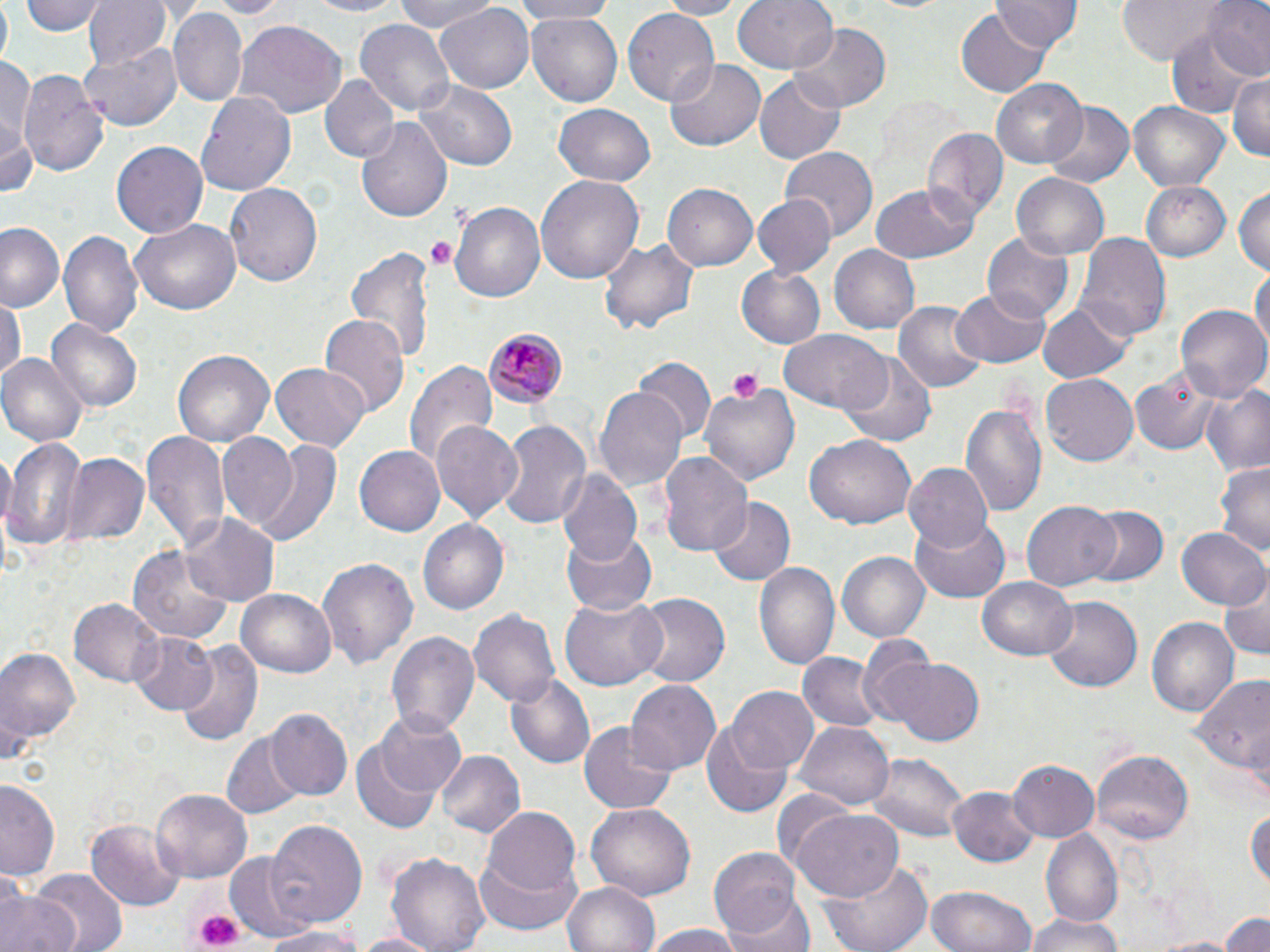
slide-level diagnosis = Plasmodium malariae
stain = May-Grünwald-Giemsa
field of view = one of a larger specimen
preparation = thin blood smear
magnification = 1000x
Plasmodium malariae-infected red blood cell locations = approximate bounding boxes as (x1,y1)-(x2,y2) corner pairs in pixels: (482,326)-(566,409)
modality = light microscopy
platelet locations = approximate bounding boxes as (x1,y1)-(x2,y2) corner pairs in pixels: (425,235)-(459,270), (726,368)-(762,402), (191,905)-(243,949)
image size = 1270×952 pixels
uninfected red blood cell locations = approximate bounding boxes as (x1,y1)-(x2,y2) corner pairs in pixels: (23,0)-(105,37), (83,0)-(169,71), (199,0)-(293,18), (296,0)-(411,17), (393,0)-(497,33), (508,0)-(625,22), (658,0)-(741,18), (733,0)-(838,75), (993,0)-(1081,54), (1115,0)-(1225,65), (1202,0)-(1270,80), (436,3)-(532,92), (171,7)-(248,107), (957,7)-(1052,95), (624,9)-(721,107), (527,12)-(623,109), (235,19)-(347,119), (355,19)-(454,114), (1166,22)-(1258,114), (791,25)-(891,111), (80,40)-(181,133), (0,57)-(33,146), (666,58)-(765,151), (19,68)-(108,177), (1225,72)-(1270,160), (756,73)-(846,165), (320,74)-(397,165), (991,77)-(1089,168), (414,78)-(516,171), (196,89)-(297,197), (1128,100)-(1230,191), (1041,103)-(1134,190), (551,104)-(657,188), (2,112)-(37,200), (357,117)-(452,225), (922,126)-(1006,225), (112,140)-(208,240), (780,146)-(879,239), (1012,172)-(1111,260), (536,173)-(642,284), (226,180)-(323,289), (1142,180)-(1229,261), (870,182)-(981,264), (664,185)-(757,271), (1233,185)-(1270,279), (753,196)-(834,276), (451,201)-(545,305), (130,220)-(242,315), (1,224)-(65,311), (58,228)-(143,339), (983,233)-(1076,319), (598,234)-(699,338), (1076,234)-(1169,345), (345,245)-(437,364), (829,246)-(920,334), (1253,265)-(1269,360), (736,266)-(826,349), (949,287)-(1049,369), (0,294)-(23,387), (1037,301)-(1133,384), (894,302)-(985,395), (1176,303)-(1269,400), (319,314)-(409,419), (48,320)-(144,413), (778,329)-(891,412), (174,347)-(274,447), (838,352)-(941,448), (0,354)-(87,449), (632,358)-(714,445), (404,361)-(495,470), (270,362)-(371,451), (1128,363)-(1230,456), (1040,374)-(1138,466), (700,380)-(800,488), (1201,383)-(1270,477), (595,387)-(689,493), (962,403)-(1046,513), (495,419)-(592,533), (431,420)-(525,519), (139,430)-(232,551), (215,431)-(300,523), (805,432)-(918,530), (229,434)-(342,548), (4,439)-(85,551), (355,448)-(445,535), (659,451)-(753,561), (62,454)-(148,548), (903,462)-(992,553), (1216,463)-(1269,559), (556,470)-(642,566), (710,497)-(794,587), (1023,500)-(1121,589), (1080,504)-(1168,588), (185,515)-(278,604), (910,515)-(1011,601), (419,519)-(508,614), (1176,526)-(1267,612), (560,527)-(660,616), (130,543)-(234,642), (835,550)-(928,643), (317,556)-(416,674), (755,559)-(841,673), (1220,572)-(1270,661), (978,575)-(1076,660), (236,588)-(337,678), (635,592)-(730,687), (1043,594)-(1142,694), (560,597)-(666,690), (71,598)-(163,689), (469,607)-(560,707), (1147,616)-(1238,714), (387,627)-(479,737), (129,630)-(220,716), (857,636)-(940,726), (173,639)-(264,751), (0,643)-(82,753), (799,650)-(884,732), (884,658)-(983,744), (1184,669)-(1268,789), (504,673)-(595,769), (626,679)-(720,776), (729,685)-(815,769), (265,710)-(352,802), (373,710)-(468,797), (701,720)-(794,818), (580,721)-(677,814), (796,721)-(894,809), (221,730)-(306,819), (352,739)-(446,836), (436,749)-(526,838), (1091,750)-(1193,843), (866,751)-(973,842), (1008,761)-(1100,842), (1,778)-(63,880), (151,788)-(251,884), (949,788)-(1037,867), (587,802)-(694,902), (1246,804)-(1269,892), (482,806)-(581,902), (793,808)-(904,904), (86,818)-(183,912), (264,819)-(369,928), (1043,831)-(1124,923), (709,846)-(803,941), (385,849)-(490,952), (227,852)-(311,943), (476,852)-(581,935), (818,858)-(934,952), (26,867)-(125,952), (562,881)-(659,952), (925,884)-(1041,952), (0,887)-(78,952), (723,893)-(816,952), (1220,909)-(1270,952), (1024,912)-(1128,952), (255,926)-(367,952), (640,926)-(747,952), (352,932)-(441,952), (1145,935)-(1247,951)